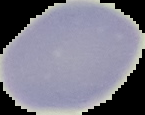 From a thin blood smear. Malaria status: uninfected. Image is 145×115 pixels. The area outside the segmented cell region is set to black.